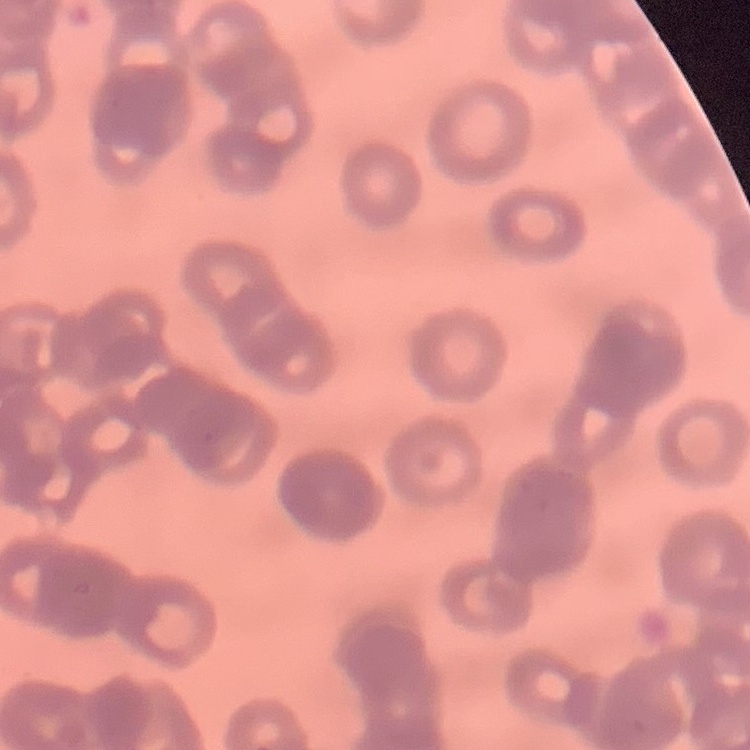

The erythrocytes exhibit rouleaux formation. Stained with either Field's or Giemsa. Square crop of a larger photomicrograph. Thin blood smear.